Locate every malaria parasite.
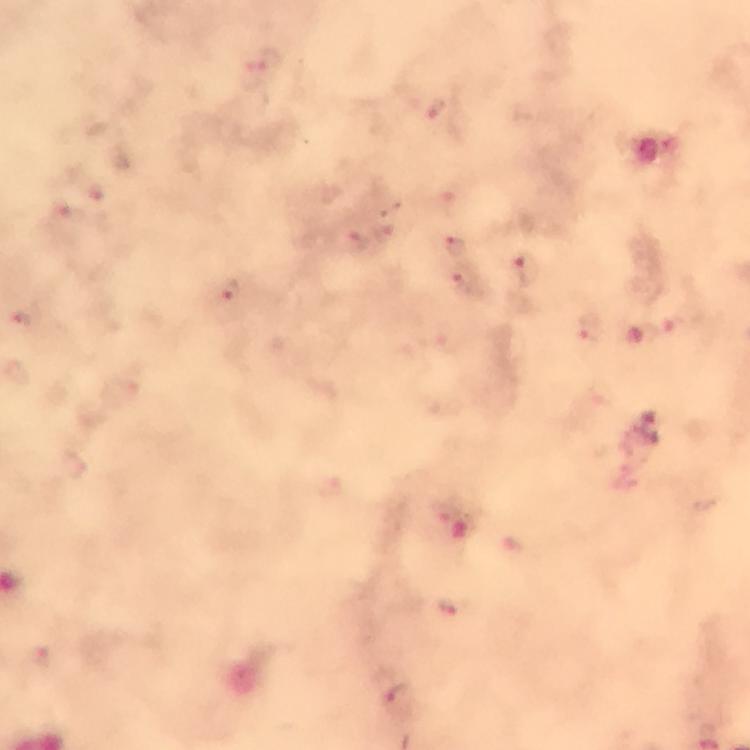

Approximate centers as (x, y) in pixels.
Malaria parasites: (388, 233), (358, 240), (456, 244), (528, 272), (467, 283), (230, 289), (19, 321), (588, 328), (452, 606), (396, 699).

Summary:
  - Image size: 750×750 pixels
  - Stain: Giemsa
  - Cropped from: one field of view
  - Preparation: thick blood smear
  - Capture: smartphone mounted on the microscope
  - Immersion oil: applied
  - Context: from a diagnostic examination for malaria
  - Magnification: 100x